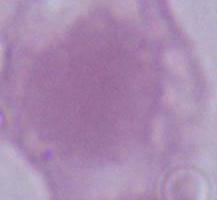 Micrograph. 1000x magnification. A red blood cell is shown.